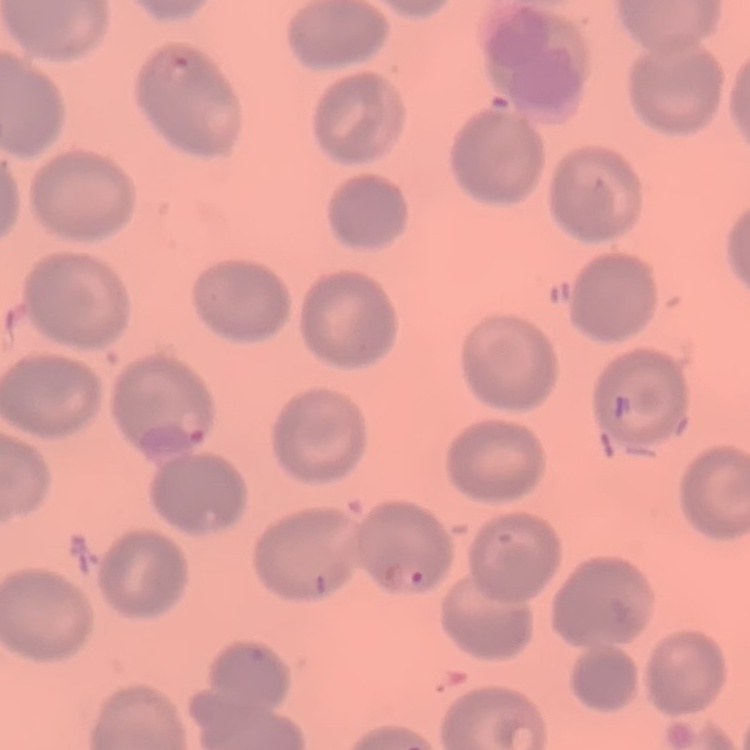
Summary:
  - Red blood cell morphology: no rouleaux formation
  - Image type: one tile cut from a larger photomicrograph
  - Preparation: thin peripheral smear
  - Stain: Field's or Giemsa